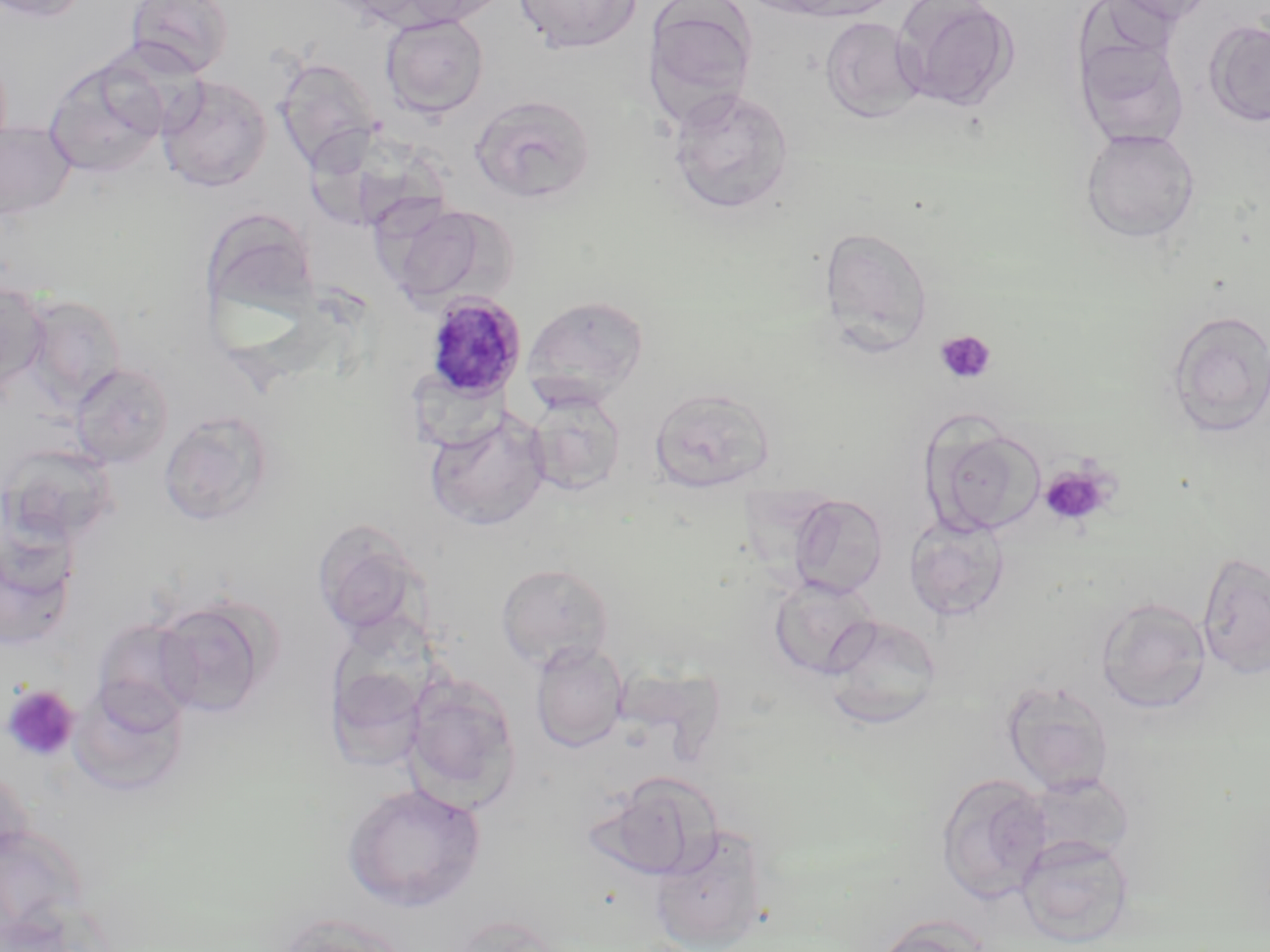
slide-level diagnosis = Plasmodium malariae
magnification = 1000x
image size = 1270×952 pixels
Plasmodium malariae-infected red blood cell locations = approximate bounding boxes as (x1, y1, x2, y2) in pixels: (424, 292, 526, 401)
platelet locations = approximate bounding boxes as (x1, y1, x2, y2) in pixels: (935, 330, 997, 384), (1039, 464, 1115, 528), (2, 684, 80, 762)
uninfected red blood cell locations = approximate bounding boxes as (x1, y1, x2, y2) in pixels: (0, 0, 91, 23), (126, 0, 234, 77), (390, 0, 513, 27), (514, 0, 642, 54), (765, 0, 903, 21), (893, 0, 1019, 112), (1106, 0, 1220, 26), (642, 1, 758, 128), (380, 13, 489, 118), (819, 16, 926, 122), (1205, 19, 1270, 127), (1077, 37, 1190, 149), (274, 56, 382, 172), (43, 57, 167, 179), (156, 74, 272, 193), (667, 87, 794, 215), (470, 93, 596, 205), (0, 121, 76, 219), (1081, 128, 1200, 243), (383, 201, 506, 310), (818, 226, 933, 355), (0, 278, 49, 394), (20, 294, 126, 410), (523, 294, 649, 408), (1166, 310, 1270, 437), (69, 362, 175, 469), (649, 386, 774, 493), (526, 391, 627, 496), (158, 409, 276, 527), (425, 409, 551, 532), (925, 422, 1047, 537), (0, 442, 121, 547), (788, 494, 888, 597), (905, 514, 1010, 621), (0, 517, 79, 654), (312, 519, 427, 639), (1197, 551, 1270, 679), (496, 562, 615, 671), (769, 576, 879, 679), (151, 596, 274, 718), (1096, 597, 1212, 713), (823, 614, 941, 729), (92, 617, 199, 725), (530, 641, 628, 752), (325, 650, 432, 774), (612, 666, 720, 749), (403, 672, 522, 810), (68, 678, 190, 798), (1002, 680, 1115, 795), (935, 771, 1052, 904), (591, 772, 720, 881), (1025, 773, 1135, 863), (342, 782, 486, 912), (1, 823, 89, 939), (650, 824, 771, 952), (1016, 834, 1134, 946), (272, 913, 413, 952), (873, 916, 988, 952)
field of view = single
stain = May-Grünwald-Giemsa
preparation = thin blood film
modality = light microscopy